Name the parasite shown.
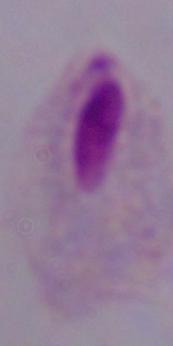
A trichomonad.

magnification = 1000x
modality = photomicrograph